Describe the morphology of the erythrocytes.
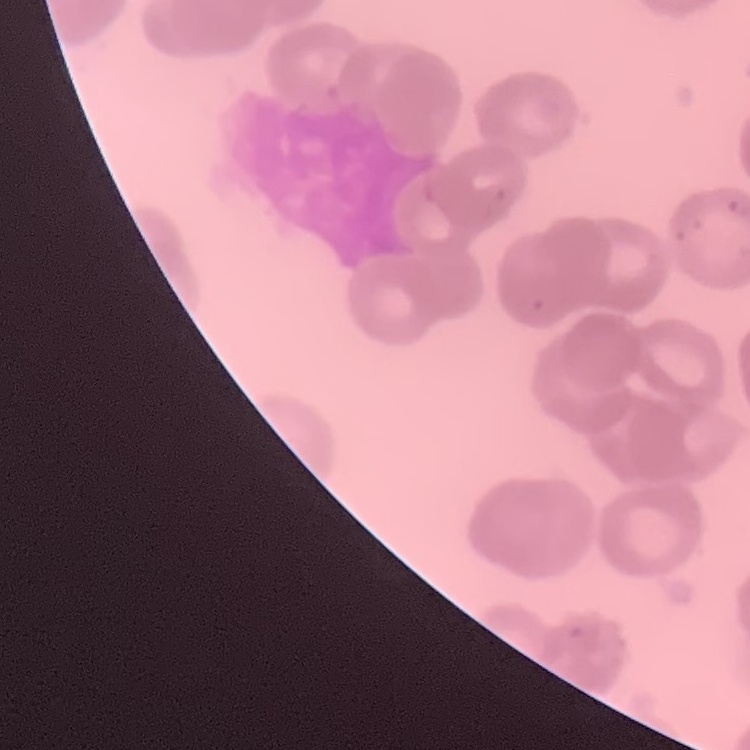
They show rouleaux formation.

preparation = thin blood film
image type = square crop of a larger photomicrograph
stain = Field's or Giemsa